Assess this cell for malaria.
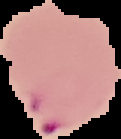
It is parasitized.

Summary:
  - Image size: 121×139 pixels
  - Preparation: thin blood film
  - Image type: segmented cell region on a black background